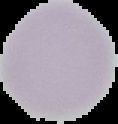

{
  "image_size": "118×124 pixels",
  "preparation": "thin blood film",
  "result": "no Plasmodium parasites detected",
  "image_type": "segmented cell region on a black background"
}